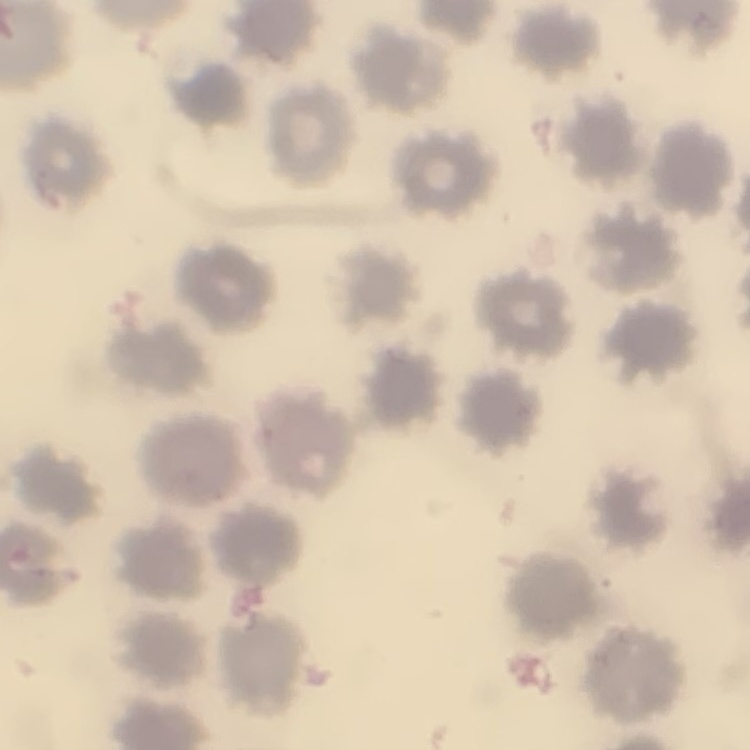

The erythrocytes show no rouleaux formation. Field's or Giemsa stain. One tile cut from a larger photomicrograph. Thin blood film.